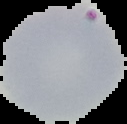
result = Plasmodium parasites detected
preparation = thin blood smear
image size = 127×124 pixels
image type = cell region segmented out of the field of view; surrounding area masked to black